Look for Plasmodium parasites.
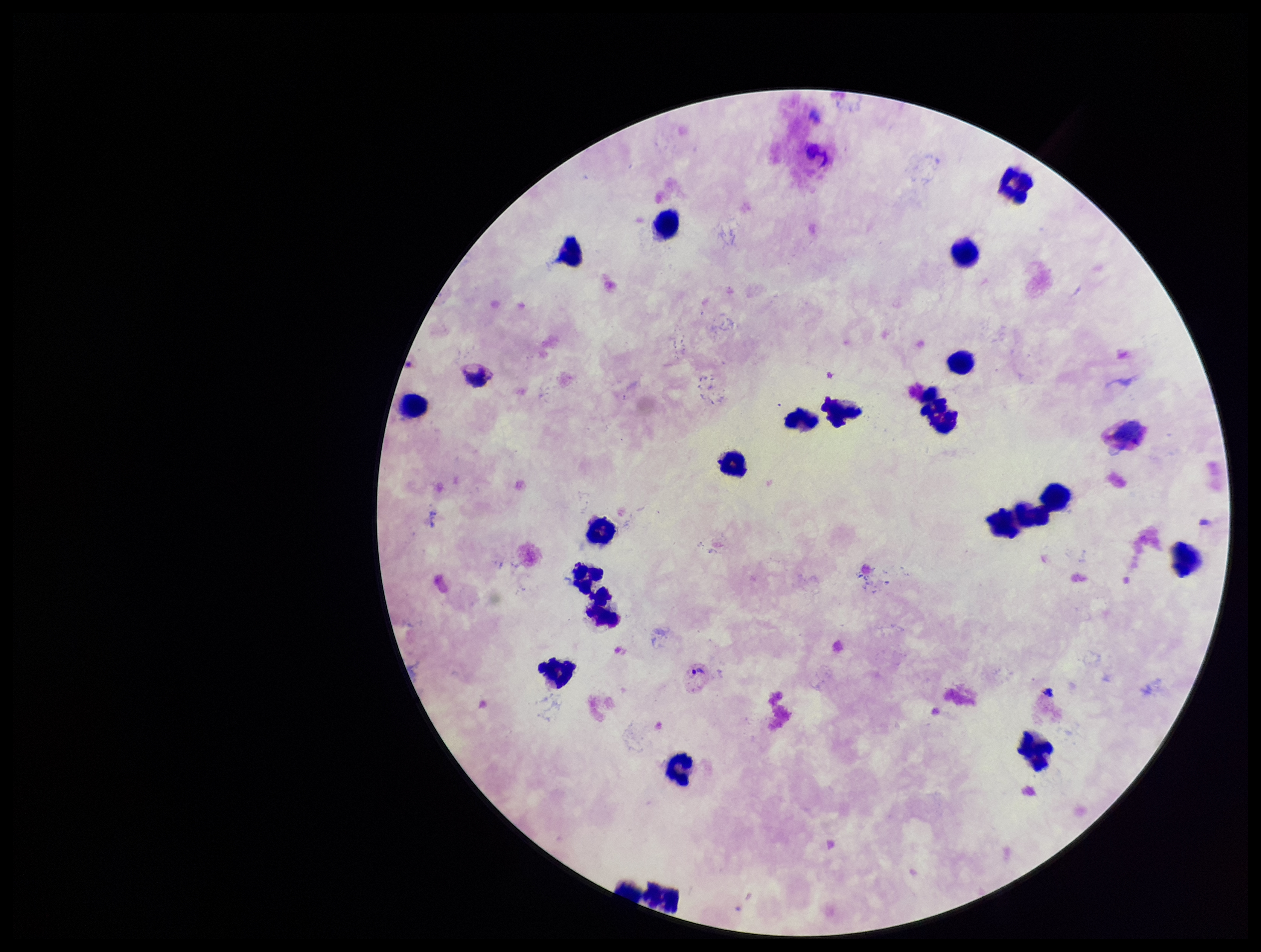

Detected.

preparation: thick
species_reported_for_this_patient: Plasmodium vivax
parasite_count: 1
leukocyte_count: 21
field_of_view: single
patient_malaria_status: positive
image_size: 1261×952 pixels
capture: smartphone photograph through the microscope eyepiece
stain: Giemsa